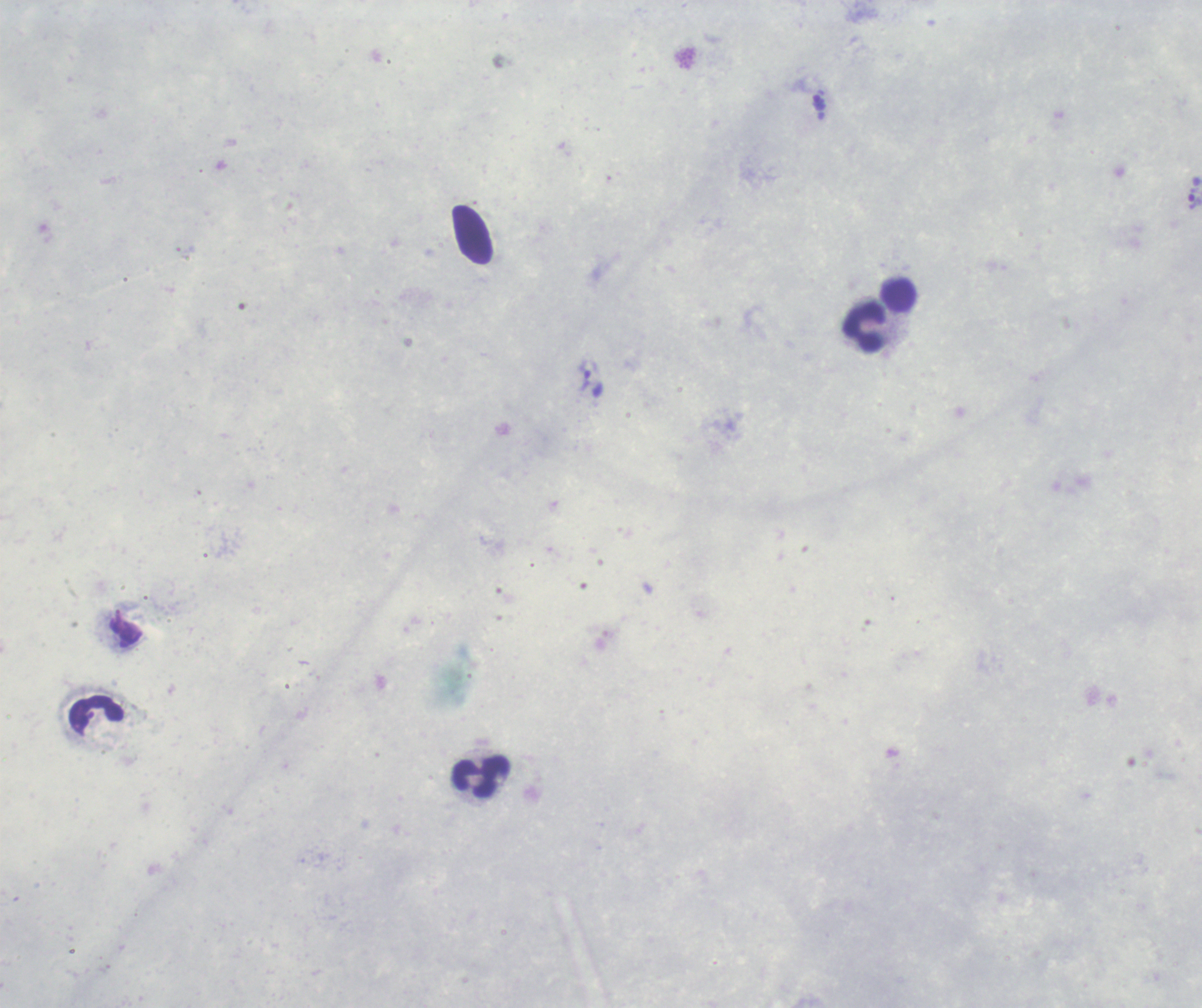

coordinate format = approximate centers as {x, y} in pixels
trophozoite locations = {1195, 198}, {584, 376}
leukocyte locations = {898, 296}, {865, 329}, {98, 715}, {481, 777}
field of view = one from this slide
context = previously used in a real diagnosis
background quality = unsatisfactory
image size = 1202×1008 pixels
preparation = thick blood smear
result = Plasmodium parasites detected
magnification = 100x
stain = Romanowsky